Locate every blood parasite and identify its species.
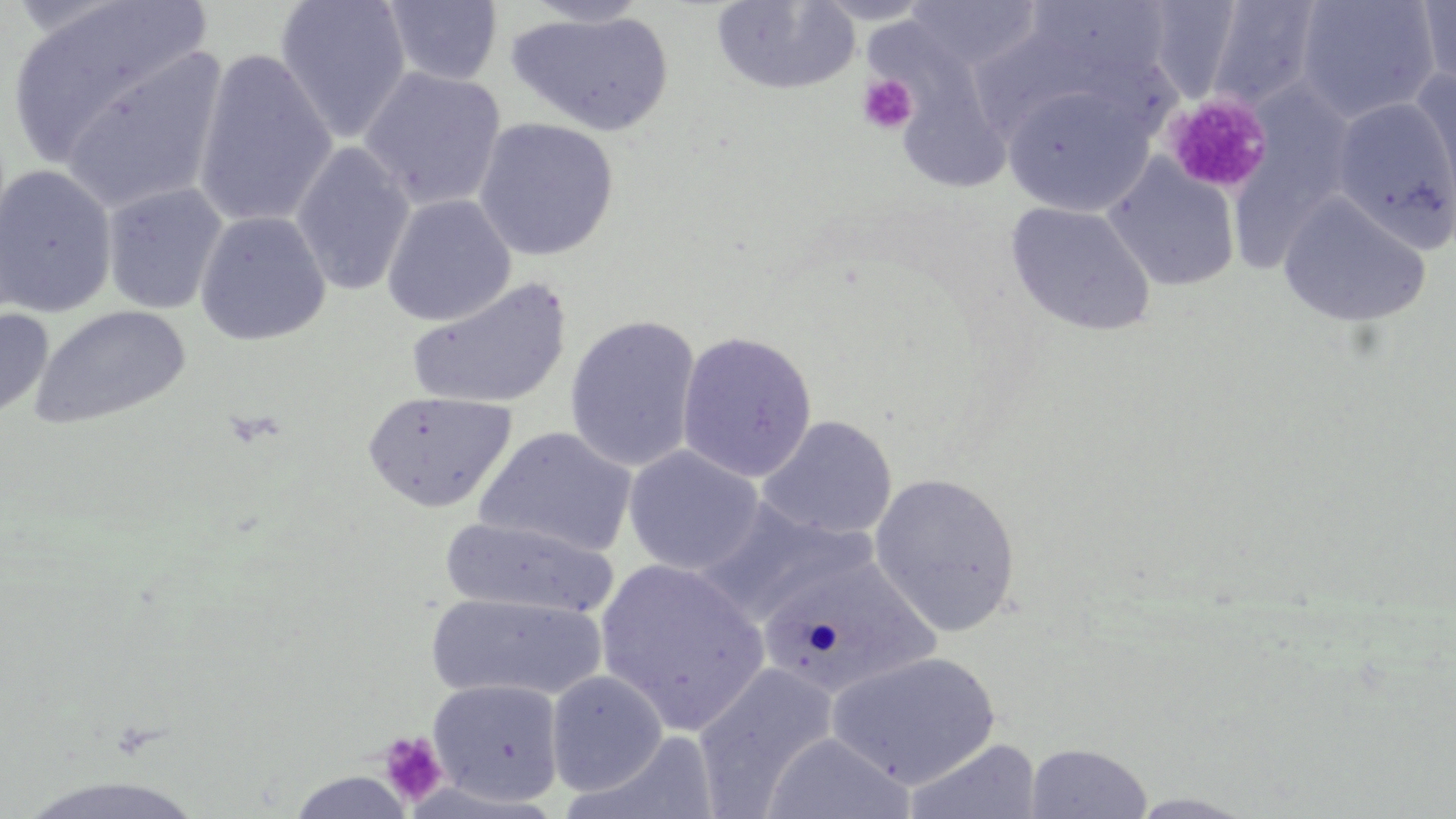

No blood parasites observed.

Approximate bounding boxes as (x1,y1)-(x2,y2) corner pairs in pixels. Platelet locations: (856,73)-(920,135), (1166,93)-(1272,195), (377,731)-(448,807). Uninfected red blood cell locations: (5,0)-(216,169), (274,0)-(412,144), (382,0)-(504,86), (806,0)-(939,25), (1295,0)-(1440,123), (1416,0)-(1456,90), (519,1)-(654,27), (710,1)-(860,96), (1015,1)-(1177,91), (1204,1)-(1325,109), (900,2)-(1046,74), (506,10)-(674,137), (962,16)-(1133,145), (53,43)-(230,216), (192,48)-(337,231), (358,67)-(507,211), (1409,70)-(1456,219), (1002,81)-(1158,217), (1234,88)-(1353,271), (1332,97)-(1456,250), (473,118)-(620,261), (291,141)-(415,297), (1102,156)-(1241,293), (0,165)-(117,318), (102,182)-(228,315), (1277,193)-(1432,327), (382,194)-(516,327), (1004,201)-(1156,336), (195,210)-(331,346), (405,276)-(573,410), (30,305)-(192,430), (0,307)-(54,424), (564,314)-(702,473), (676,331)-(818,482), (363,389)-(517,512), (758,415)-(897,540), (474,426)-(637,558), (623,445)-(765,576), (869,472)-(1022,638), (694,500)-(876,625), (440,516)-(617,620), (757,554)-(939,700), (594,559)-(770,733), (425,592)-(606,703), (826,651)-(1001,789), (693,662)-(839,814), (546,670)-(668,796), (427,678)-(565,807), (762,733)-(914,819), (902,738)-(1043,819), (1024,742)-(1153,818), (286,770)-(417,817), (15,774)-(208,819), (1125,791)-(1259,818). Slide-level diagnosis: negative for blood parasites. Optical microscopy. May-Grünwald-Giemsa stain. Thin blood film. Image is 1456×819 pixels. Captured at 1000x magnification. One field of a larger specimen.